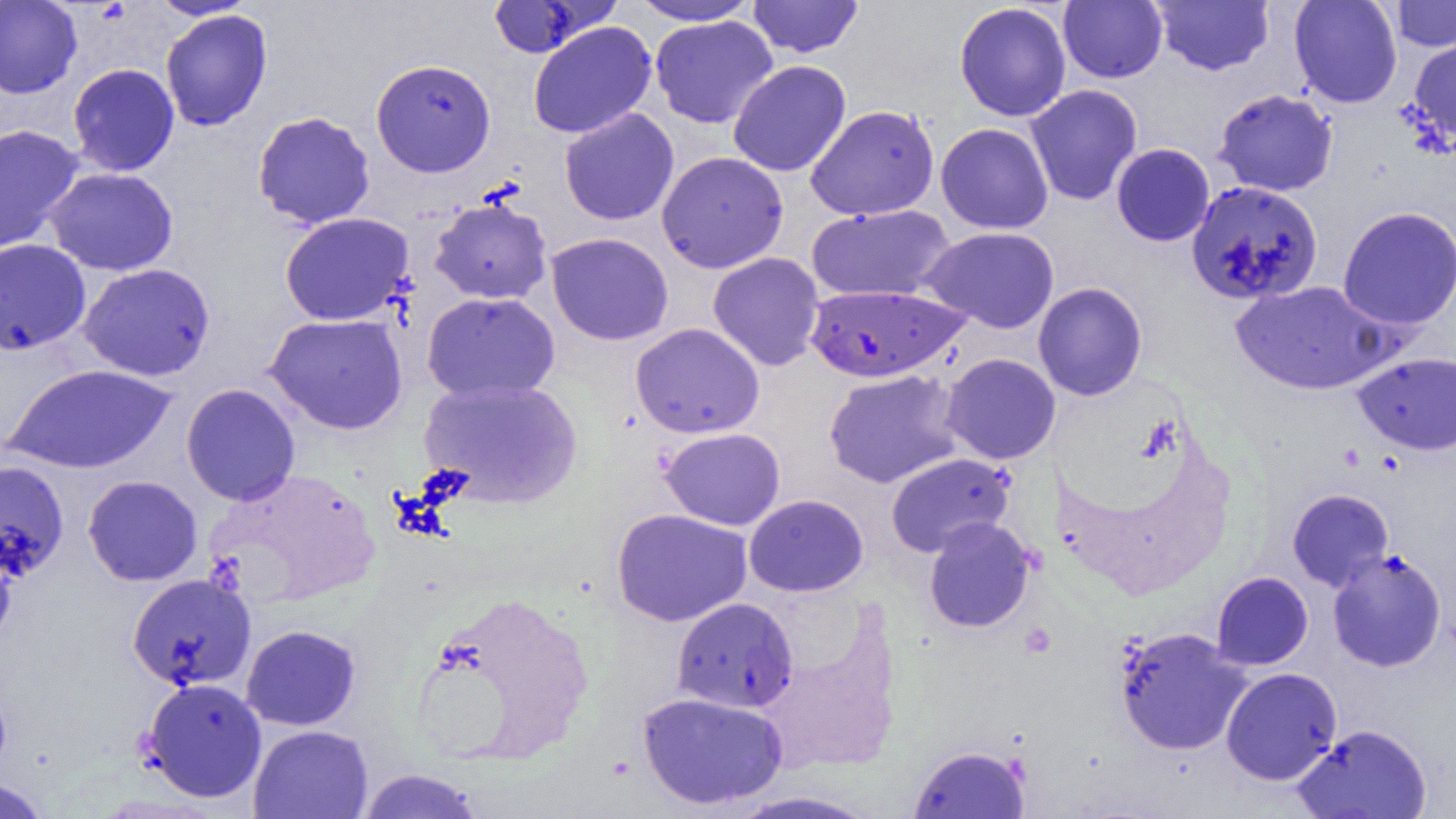

slide-level diagnosis = Plasmodium falciparum
image size = 1456×819 pixels
Plasmodium falciparum-infected red blood cell locations = approximate bounding boxes as [x1, y1, x2, y2] in pixels: [804, 283, 969, 383]
magnification = 1000x
preparation = thin blood smear
modality = optical microscopy
uninfected red blood cell locations = approximate bounding boxes as [x1, y1, x2, y2] in pixels: [627, 0, 761, 25], [747, 0, 863, 58], [1151, 0, 1274, 76], [1289, 0, 1402, 108], [1390, 0, 1456, 52], [0, 1, 82, 99], [150, 1, 259, 21], [486, 1, 614, 58], [1058, 1, 1168, 84], [954, 3, 1072, 121], [160, 9, 272, 131], [650, 15, 778, 129], [528, 21, 657, 139], [1408, 35, 1456, 148], [371, 58, 496, 177], [727, 60, 851, 177], [67, 63, 180, 176], [1025, 84, 1143, 206], [1214, 88, 1338, 196], [805, 104, 939, 220], [559, 108, 679, 226], [252, 111, 375, 229], [935, 122, 1054, 234], [0, 124, 84, 254], [1111, 143, 1215, 246], [657, 151, 788, 273], [44, 167, 178, 276], [1185, 180, 1324, 305], [429, 195, 553, 304], [806, 204, 955, 302], [1337, 206, 1456, 330], [280, 212, 414, 325], [919, 226, 1060, 333], [546, 232, 673, 346], [0, 238, 91, 355], [708, 252, 825, 371], [78, 262, 215, 381], [1231, 280, 1391, 395], [1033, 282, 1147, 401], [422, 292, 560, 403], [265, 313, 408, 435], [630, 322, 764, 439], [1353, 352, 1456, 455], [941, 353, 1061, 465], [4, 364, 177, 474], [823, 369, 964, 489], [419, 377, 582, 508], [181, 384, 300, 506], [660, 427, 786, 530], [885, 452, 1015, 557], [0, 461, 68, 579], [83, 475, 203, 586], [1287, 488, 1394, 591], [744, 494, 868, 597], [611, 508, 752, 626], [923, 516, 1035, 633], [0, 536, 16, 650], [1327, 548, 1447, 672], [1214, 571, 1320, 779], [1211, 572, 1313, 670], [126, 573, 256, 691], [412, 589, 597, 768], [672, 597, 798, 712], [241, 624, 360, 730], [1114, 626, 1252, 756], [1221, 667, 1342, 785], [140, 677, 267, 802], [637, 691, 789, 810], [1293, 723, 1432, 819], [249, 724, 373, 818], [909, 745, 1030, 818], [356, 768, 487, 819], [0, 778, 52, 819], [726, 790, 880, 819]
field of view = one of a larger specimen